State the blood parasite species.
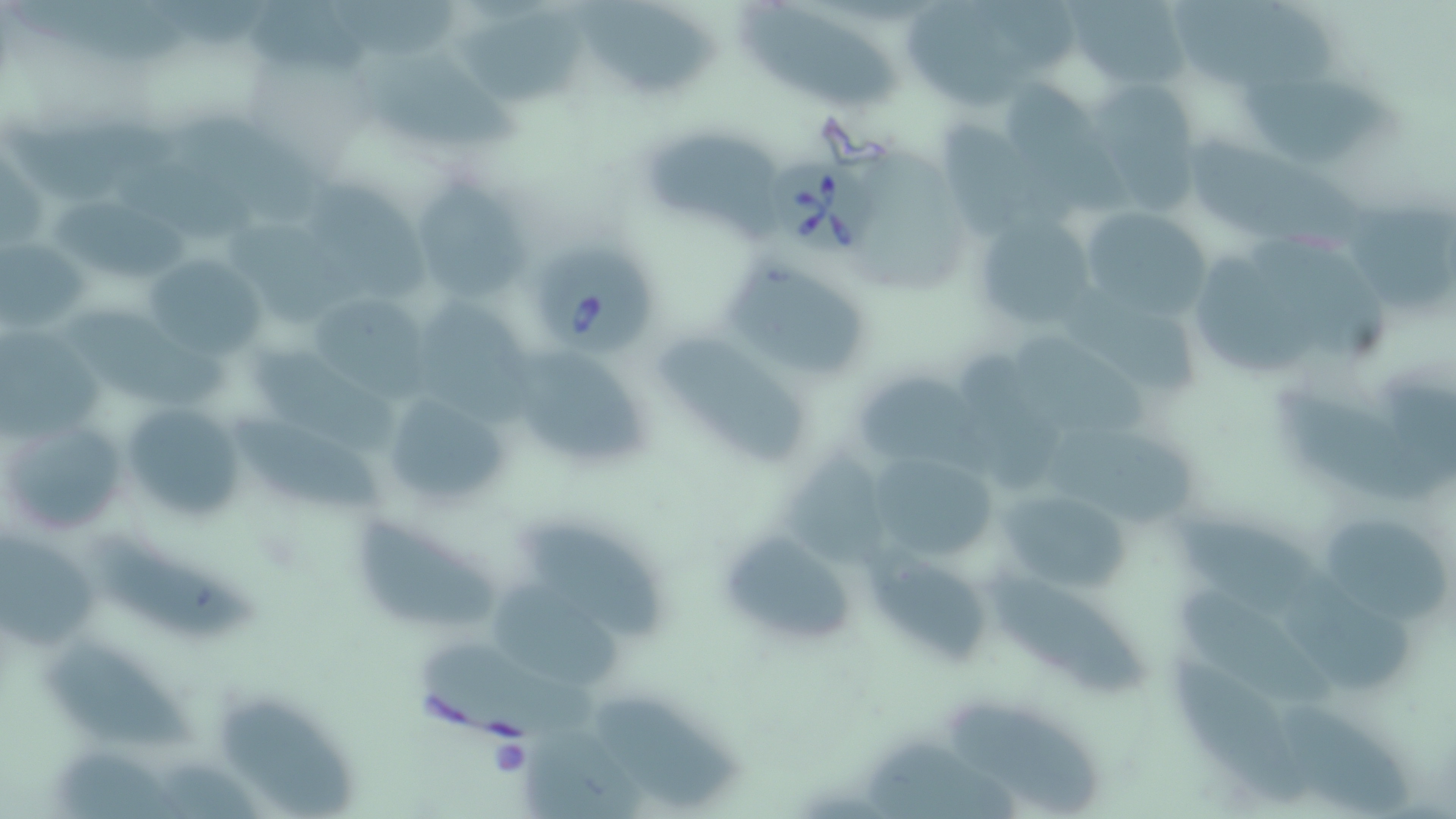

Babesia divergens.

Summary:
  - Coordinate format: approximate bounding boxes as (x1, y1, x2, y2) in pixels
  - Platelet locations: (487, 734, 531, 779)
  - Uninfected red blood cell locations: (334, 0, 469, 62), (578, 0, 721, 100), (1068, 0, 1190, 85), (1177, 2, 1357, 99), (248, 4, 381, 72), (908, 4, 1046, 111), (458, 5, 587, 103), (743, 5, 897, 110), (365, 45, 525, 146), (1240, 79, 1400, 168), (999, 80, 1093, 173), (1090, 83, 1212, 217), (4, 114, 173, 202), (938, 115, 1050, 237), (164, 118, 319, 228), (649, 129, 786, 243), (1190, 141, 1377, 252), (403, 170, 535, 303), (306, 181, 429, 308), (1342, 194, 1455, 314), (50, 197, 205, 279), (1078, 205, 1214, 326), (974, 212, 1101, 337), (222, 221, 378, 324), (1259, 234, 1396, 362), (1, 240, 88, 334), (146, 253, 266, 364), (1197, 256, 1318, 379), (724, 263, 862, 371), (303, 291, 442, 401), (1062, 291, 1207, 398), (418, 300, 540, 424), (66, 303, 232, 409), (0, 327, 99, 444), (1011, 334, 1152, 436), (658, 342, 815, 468), (499, 344, 652, 472), (251, 348, 399, 458), (959, 352, 1077, 480), (851, 368, 979, 466), (380, 388, 516, 515), (1279, 391, 1455, 505), (120, 400, 250, 522), (227, 409, 383, 512), (1, 417, 128, 540), (1043, 426, 1205, 527), (783, 448, 898, 574), (864, 449, 1006, 566), (994, 485, 1140, 595), (358, 515, 501, 629), (1180, 515, 1323, 622), (1325, 519, 1453, 625), (718, 526, 861, 651), (528, 527, 669, 639), (0, 532, 101, 651), (94, 536, 257, 639), (873, 552, 993, 664), (1283, 568, 1413, 690), (981, 570, 1153, 698), (493, 576, 626, 688), (1174, 588, 1339, 708), (48, 645, 209, 747), (1160, 646, 1314, 808), (425, 650, 602, 736), (599, 690, 745, 807), (1276, 696, 1421, 816), (218, 701, 361, 819), (952, 705, 1103, 815), (523, 733, 664, 819), (853, 744, 1024, 819), (54, 748, 194, 818)
  - Babesia divergens-infected red blood cell locations: (772, 157, 879, 261), (528, 245, 660, 355)
  - Modality: light microscopy
  - Image size: 1456×819 pixels
  - Stain: May-Grünwald-Giemsa
  - Magnification: 1000x
  - Preparation: thin blood smear
  - Field of view: single